Classify this cell by malaria status.
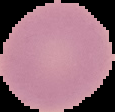

It is uninfected.

preparation = thin blood smear
image type = cell region segmented out of the field of view; surrounding area masked to black
image size = 115×112 pixels